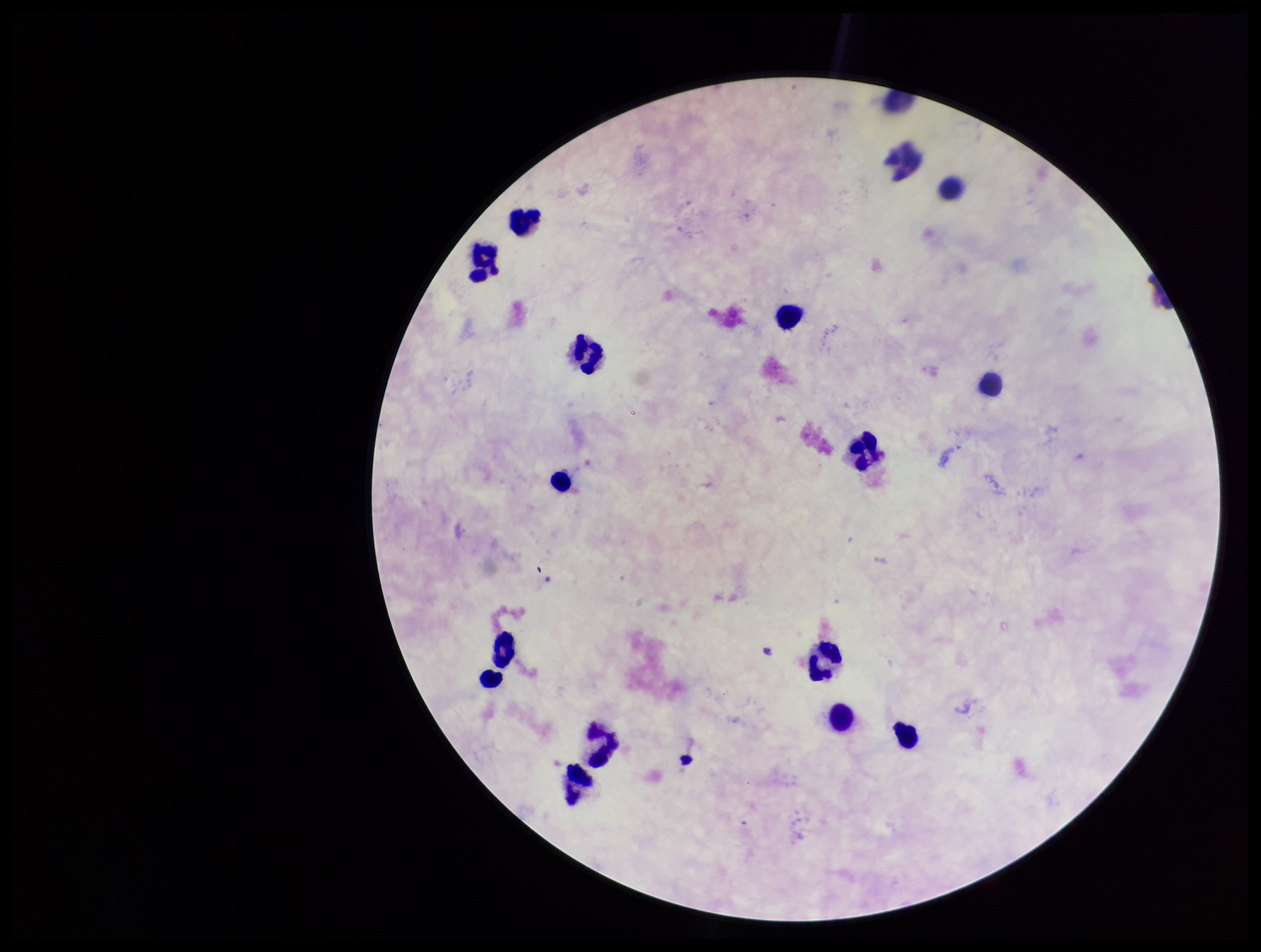

Preparation: thick. Patient malaria status: negative. Photographed through the microscope eyepiece with a smartphone camera. Stained with Giemsa. Parasite count: 0. One field from this slide. Image is 1261×952 pixels. Leukocyte count: 15. Plasmodium parasites: none detected.